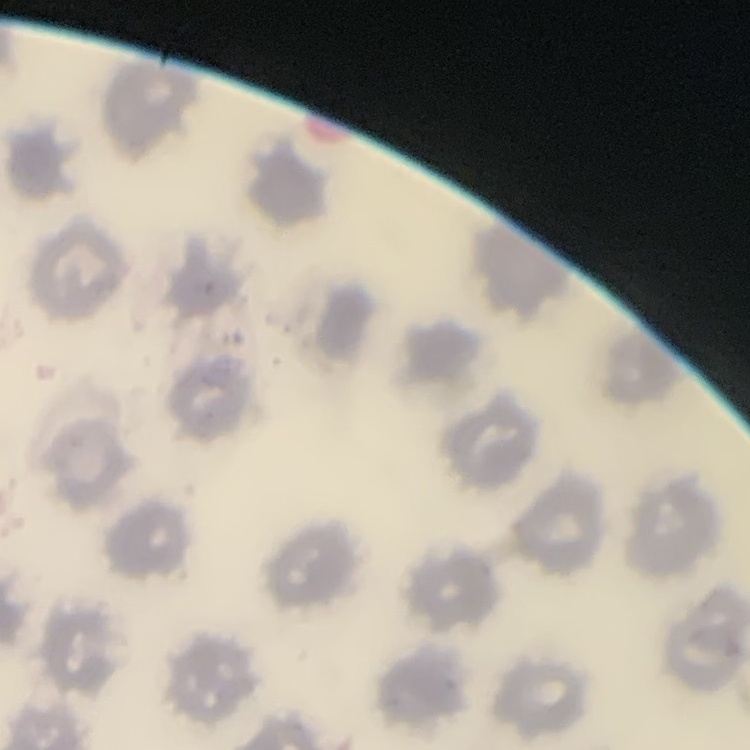
The red blood cells exhibit no rouleaux formation. Square crop of a larger photomicrograph. Thin blood smear. Stained with either Field's or Giemsa.